Assess the morphology of the red blood cells.
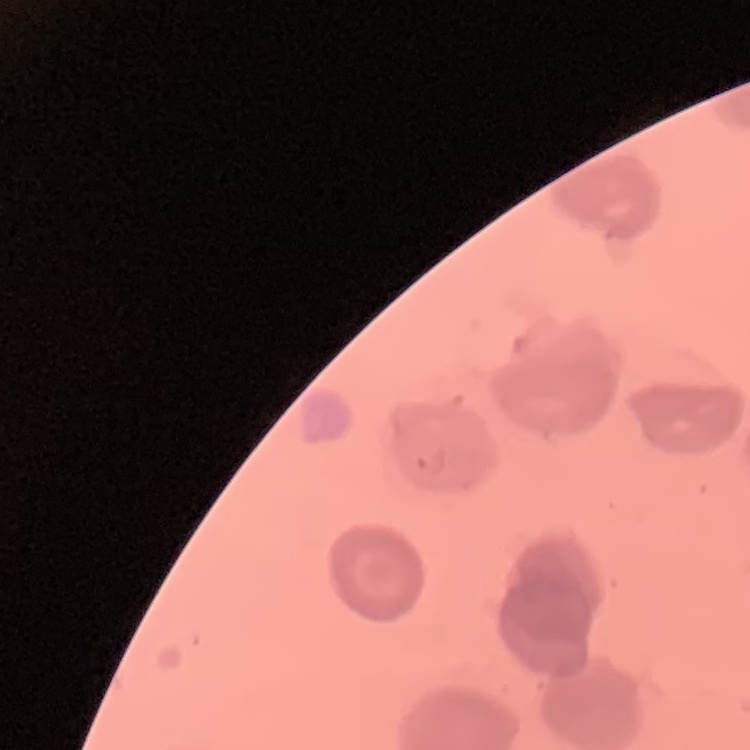
No rouleaux formation.

Summary:
  - Stain: Field's or Giemsa
  - Preparation: thin peripheral smear
  - Image type: one tile cut from a larger photomicrograph